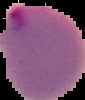

image type = segmented cell region with the area outside set to black
result = Plasmodium parasites detected
preparation = thin blood smear
image size = 85×100 pixels